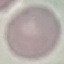

malaria status = uninfected
stain = Giemsa
capture = smartphone camera at the microscope eyepiece
preparation = thin smear
image type = cell patch, automatically extracted from a larger field of view and resized to 64 × 64 pixels